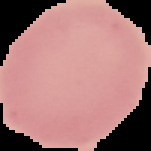
From a thin blood smear. Result: negative for Plasmodium parasites. The area outside the segmented cell region is set to black. Image is 151×151 pixels.